Identify the blood parasite species.
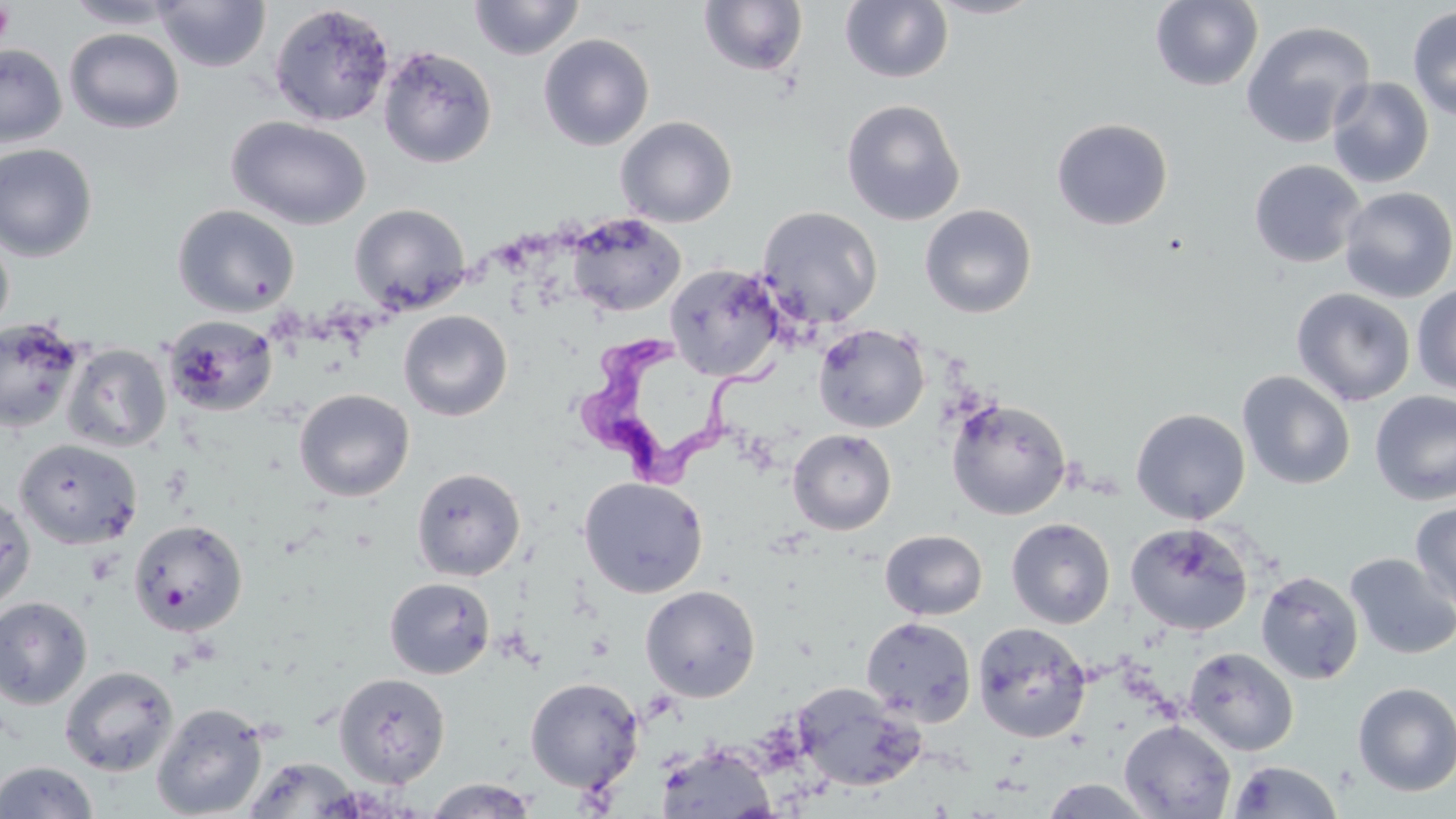
Trypanosoma brucei.

Summary:
  - Coordinate format: approximate bounding boxes as (x1, y1, x2, y2) in pixels
  - Trypanosoma brucei locations: (568, 333, 787, 489)
  - Uninfected red blood cell locations: (64, 0, 186, 29), (154, 0, 271, 73), (468, 0, 585, 60), (926, 0, 1046, 19), (1150, 0, 1263, 91), (698, 1, 808, 78), (840, 1, 953, 84), (269, 4, 395, 127), (1407, 5, 1456, 121), (1240, 20, 1376, 147), (64, 27, 185, 134), (538, 34, 655, 151), (0, 44, 67, 148), (378, 45, 498, 168), (1327, 77, 1435, 188), (841, 99, 966, 226), (226, 116, 372, 230), (615, 116, 738, 227), (1051, 117, 1173, 231), (0, 143, 98, 262), (1249, 159, 1366, 268), (1339, 186, 1456, 303), (349, 203, 471, 314), (172, 204, 301, 317), (919, 204, 1038, 319), (757, 206, 883, 330), (566, 213, 686, 317), (0, 226, 14, 344), (664, 263, 784, 381), (1412, 284, 1456, 395), (1292, 288, 1416, 407), (398, 310, 512, 421), (163, 315, 278, 416), (0, 317, 86, 434), (813, 323, 929, 433), (62, 343, 171, 453), (1237, 371, 1355, 490), (294, 388, 415, 502), (1370, 390, 1456, 505), (945, 397, 1072, 520), (1130, 408, 1251, 524), (787, 429, 896, 535), (13, 439, 143, 549), (411, 467, 526, 581), (578, 476, 708, 598), (0, 491, 36, 612), (1410, 502, 1456, 613), (1006, 517, 1116, 629), (128, 518, 248, 636), (1125, 522, 1253, 636), (880, 529, 987, 621), (1345, 552, 1456, 660), (1256, 570, 1364, 684), (384, 576, 495, 679), (640, 585, 761, 702), (0, 596, 93, 710), (860, 616, 976, 726), (972, 622, 1092, 743), (1183, 647, 1298, 756), (59, 665, 178, 777), (334, 673, 451, 788), (525, 677, 644, 793), (1352, 681, 1456, 796), (791, 683, 925, 792), (151, 702, 269, 818), (1119, 719, 1235, 819), (655, 745, 777, 819), (241, 756, 366, 818), (0, 760, 98, 818), (1228, 760, 1343, 818), (423, 778, 537, 818), (1036, 778, 1159, 818)
  - Platelet locations: (0, 4, 15, 47)
  - Image size: 1456×819 pixels
  - Preparation: thin blood smear
  - Stain: May-Grünwald-Giemsa
  - Modality: optical microscopy
  - Magnification: 1000x
  - Field of view: single